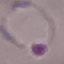
Summary:
  - Result: malaria parasites identified
  - Stain: Giemsa
  - Capture: smartphone through the microscope eyepiece
  - Preparation: thin smear
  - Image type: cell patch, automatically extracted from a larger field of view and resized to 64 × 64 pixels